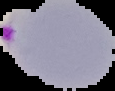
image size = 115×91 pixels
preparation = thin blood film
image type = segmented cell region with the area outside set to black
result = malaria parasites detected